Assess this cell for malaria.
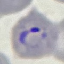

It is parasitized.

{
  "image_type": "cell patch, automatically extracted from a larger field of view and resized to 64 × 64 pixels",
  "preparation": "thin smear",
  "stain": "Giemsa",
  "capture": "smartphone camera at the microscope eyepiece"
}